State which parasite is depicted.
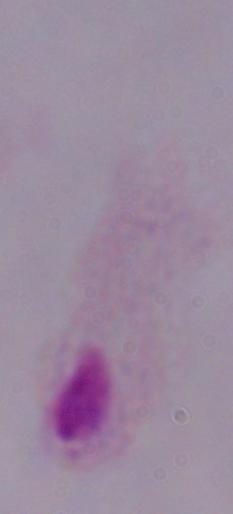
This is a trichomonad.

modality = micrograph
magnification = 1000x